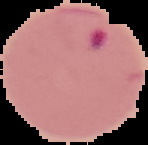
Summary:
  - Image type: segmented cell region with the area outside set to black
  - Malaria status: parasitized
  - Image size: 148×145 pixels
  - Preparation: thin blood smear